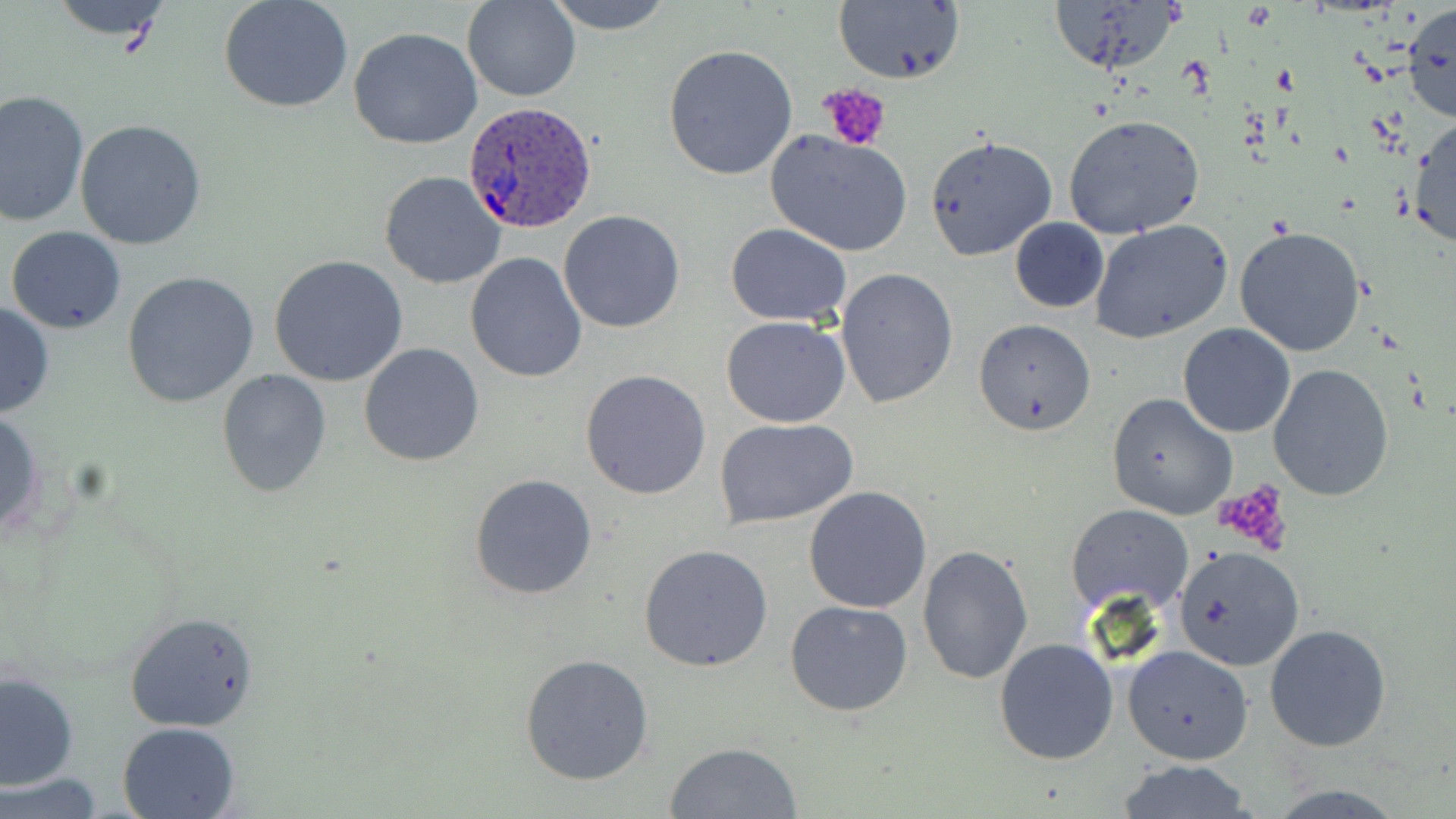
plasmodium_ovale_infected_red_blood_cell_locations: 'approximate bounding boxes as named x1/y1/x2/y2 corners in pixels: (x1=463, y1=102, x2=594, y2=233)'
slide_level_diagnosis: Plasmodium ovale
field_of_view: one of a larger specimen
stain: May-Grünwald-Giemsa
platelet_locations: 'approximate bounding boxes as named x1/y1/x2/y2 corners in pixels: (x1=818, y1=82, x2=892, y2=151), (x1=1217, y1=482, x2=1298, y2=555)'
modality: light microscopy
magnification: 1000x
preparation: thin blood smear
image_size: 1456×819 pixels
uninfected_red_blood_cell_locations: 'approximate bounding boxes as named x1/y1/x2/y2 corners in pixels: (x1=45, y1=0, x2=178, y2=43), (x1=218, y1=0, x2=354, y2=114), (x1=463, y1=0, x2=579, y2=101), (x1=543, y1=0, x2=679, y2=34), (x1=833, y1=1, x2=966, y2=87), (x1=1044, y1=1, x2=1182, y2=82), (x1=1404, y1=2, x2=1456, y2=125), (x1=346, y1=26, x2=483, y2=150), (x1=663, y1=44, x2=799, y2=181), (x1=0, y1=88, x2=90, y2=228), (x1=1407, y1=112, x2=1456, y2=254), (x1=1064, y1=113, x2=1205, y2=239), (x1=74, y1=120, x2=207, y2=251), (x1=766, y1=130, x2=913, y2=256), (x1=923, y1=135, x2=1057, y2=262), (x1=379, y1=170, x2=507, y2=289), (x1=558, y1=210, x2=687, y2=333), (x1=1009, y1=217, x2=1108, y2=313), (x1=1090, y1=220, x2=1234, y2=343), (x1=725, y1=224, x2=852, y2=327), (x1=6, y1=226, x2=127, y2=333), (x1=1234, y1=226, x2=1367, y2=357), (x1=465, y1=253, x2=587, y2=383), (x1=269, y1=256, x2=409, y2=388), (x1=836, y1=268, x2=958, y2=409), (x1=121, y1=272, x2=261, y2=409), (x1=0, y1=301, x2=54, y2=421), (x1=720, y1=316, x2=851, y2=428), (x1=974, y1=319, x2=1096, y2=436), (x1=1177, y1=323, x2=1295, y2=437), (x1=359, y1=342, x2=486, y2=467), (x1=1268, y1=364, x2=1396, y2=503), (x1=217, y1=369, x2=333, y2=499), (x1=580, y1=369, x2=712, y2=500), (x1=1107, y1=393, x2=1237, y2=520), (x1=0, y1=407, x2=44, y2=542), (x1=716, y1=418, x2=857, y2=528), (x1=469, y1=474, x2=598, y2=600), (x1=803, y1=486, x2=932, y2=613), (x1=1067, y1=503, x2=1193, y2=618), (x1=639, y1=544, x2=773, y2=671), (x1=917, y1=545, x2=1035, y2=685), (x1=1172, y1=545, x2=1304, y2=671), (x1=785, y1=600, x2=913, y2=716), (x1=123, y1=613, x2=260, y2=733), (x1=1265, y1=625, x2=1393, y2=752), (x1=994, y1=637, x2=1118, y2=764), (x1=1123, y1=645, x2=1253, y2=763), (x1=519, y1=653, x2=654, y2=787), (x1=1, y1=668, x2=78, y2=790), (x1=116, y1=721, x2=240, y2=819), (x1=662, y1=741, x2=804, y2=818), (x1=1117, y1=760, x2=1253, y2=817), (x1=1, y1=774, x2=106, y2=817), (x1=1264, y1=783, x2=1411, y2=818)'